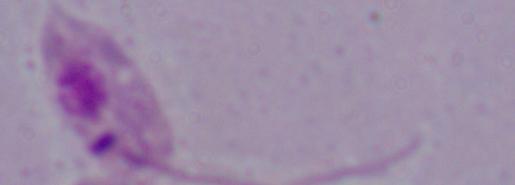
A Leishmania parasite is seen. Micrograph. Captured at 1000x magnification.